Outline each blood parasite and name the species.
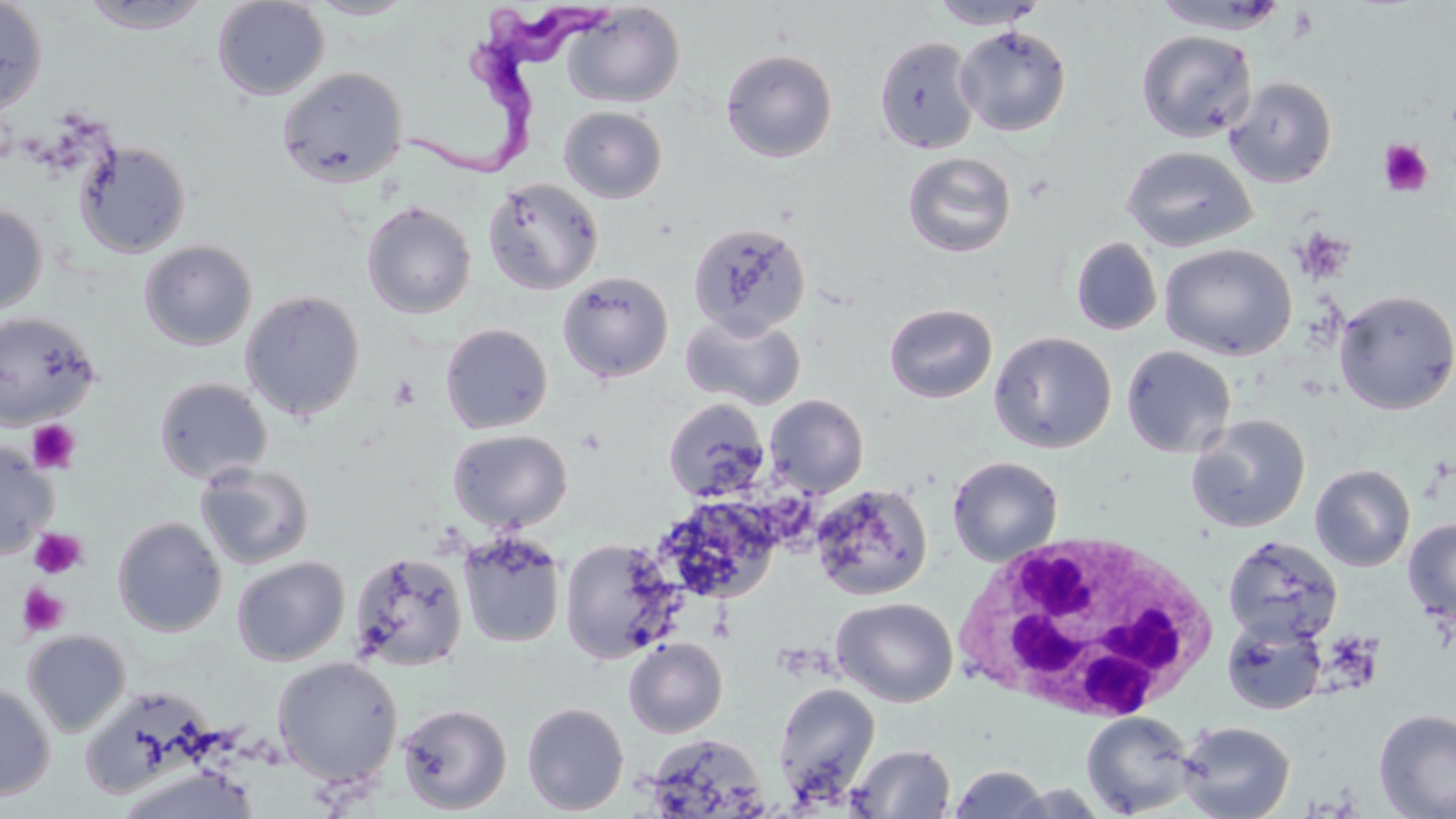
Approximate bounding boxes as named x1/y1/x2/y2 corners in pixels.
Trypanosoma brucei: (x1=401, y1=2, x2=613, y2=182).
No Plasmodium falciparum, Plasmodium ovale, Plasmodium malariae, Plasmodium vivax, or Babesia divergens observed.

{
  "slide_level_diagnosis": "Trypanosoma brucei",
  "image_size": "1456×819 pixels",
  "stain": "May-Grünwald-Giemsa",
  "magnification": "1000x",
  "platelet_locations": "approximate bounding boxes as named x1/y1/x2/y2 corners in pixels: (x1=1378, y1=140, x2=1435, y2=197), (x1=1295, y1=227, x2=1354, y2=284), (x1=388, y1=375, x2=422, y2=409), (x1=26, y1=418, x2=81, y2=475), (x1=28, y1=528, x2=87, y2=579), (x1=17, y1=583, x2=69, y2=637)",
  "preparation": "thin blood smear",
  "field_of_view": "single",
  "modality": "optical microscopy",
  "white_blood_cell_locations": "approximate bounding boxes as named x1/y1/x2/y2 corners in pixels: (x1=954, y1=527, x2=1223, y2=726)",
  "uninfected_red_blood_cell_locations": "approximate bounding boxes as named x1/y1/x2/y2 corners in pixels: (x1=0, y1=0, x2=48, y2=115), (x1=78, y1=0, x2=213, y2=34), (x1=212, y1=0, x2=330, y2=101), (x1=306, y1=0, x2=419, y2=20), (x1=928, y1=0, x2=1048, y2=30), (x1=1150, y1=0, x2=1292, y2=34), (x1=563, y1=3, x2=685, y2=108), (x1=954, y1=25, x2=1072, y2=136), (x1=1136, y1=30, x2=1257, y2=142), (x1=875, y1=36, x2=981, y2=154), (x1=721, y1=49, x2=837, y2=163), (x1=276, y1=66, x2=408, y2=188), (x1=1225, y1=76, x2=1337, y2=187), (x1=558, y1=106, x2=668, y2=203), (x1=76, y1=140, x2=191, y2=259), (x1=1121, y1=146, x2=1257, y2=252), (x1=902, y1=151, x2=1017, y2=258), (x1=482, y1=177, x2=603, y2=295), (x1=361, y1=197, x2=604, y2=310), (x1=361, y1=201, x2=477, y2=319), (x1=0, y1=203, x2=48, y2=315), (x1=687, y1=221, x2=810, y2=338), (x1=1071, y1=237, x2=1162, y2=335), (x1=138, y1=240, x2=257, y2=351), (x1=1159, y1=243, x2=1297, y2=360), (x1=557, y1=271, x2=673, y2=383), (x1=240, y1=290, x2=365, y2=421), (x1=1333, y1=290, x2=1456, y2=414), (x1=884, y1=303, x2=998, y2=403), (x1=0, y1=311, x2=101, y2=429), (x1=681, y1=312, x2=806, y2=410), (x1=440, y1=323, x2=552, y2=434), (x1=989, y1=331, x2=1117, y2=453), (x1=1120, y1=345, x2=1236, y2=458), (x1=153, y1=377, x2=272, y2=484), (x1=765, y1=394, x2=869, y2=498), (x1=662, y1=398, x2=769, y2=502), (x1=1186, y1=415, x2=1310, y2=533), (x1=447, y1=429, x2=573, y2=531), (x1=0, y1=440, x2=57, y2=558), (x1=947, y1=455, x2=1063, y2=565), (x1=195, y1=462, x2=315, y2=570), (x1=1310, y1=464, x2=1415, y2=571), (x1=811, y1=483, x2=932, y2=601), (x1=656, y1=496, x2=784, y2=604), (x1=112, y1=517, x2=227, y2=637), (x1=1403, y1=518, x2=1456, y2=623), (x1=458, y1=531, x2=566, y2=648), (x1=1223, y1=536, x2=1342, y2=646), (x1=559, y1=539, x2=682, y2=663), (x1=348, y1=551, x2=468, y2=670), (x1=232, y1=557, x2=350, y2=666), (x1=831, y1=597, x2=958, y2=707), (x1=1221, y1=617, x2=1328, y2=715), (x1=22, y1=629, x2=131, y2=737), (x1=623, y1=638, x2=727, y2=738), (x1=272, y1=657, x2=403, y2=787), (x1=0, y1=681, x2=55, y2=802), (x1=772, y1=683, x2=881, y2=802), (x1=522, y1=702, x2=629, y2=815), (x1=396, y1=703, x2=512, y2=814), (x1=1373, y1=708, x2=1456, y2=819), (x1=1081, y1=711, x2=1197, y2=817), (x1=1177, y1=721, x2=1295, y2=819), (x1=643, y1=732, x2=770, y2=818), (x1=848, y1=743, x2=956, y2=818), (x1=948, y1=765, x2=1052, y2=818), (x1=113, y1=766, x2=261, y2=819), (x1=1000, y1=783, x2=1113, y2=818)"
}